Assess the morphology of the red blood cells.
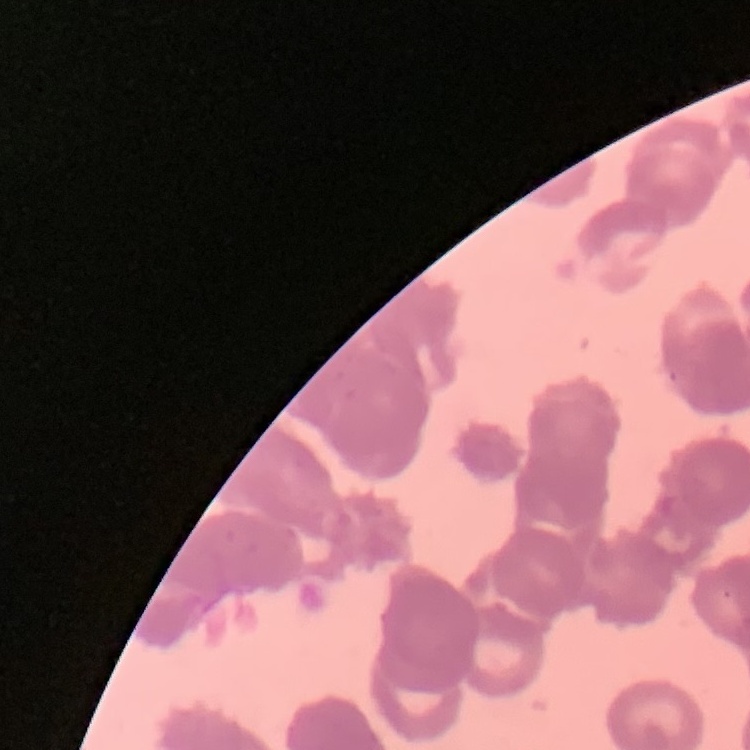
Rouleaux formation.

Summary:
  - Image type: square crop of a larger photomicrograph
  - Preparation: thin peripheral smear
  - Stain: Field's or Giemsa